Give the extent of all uninfected red blood cells.
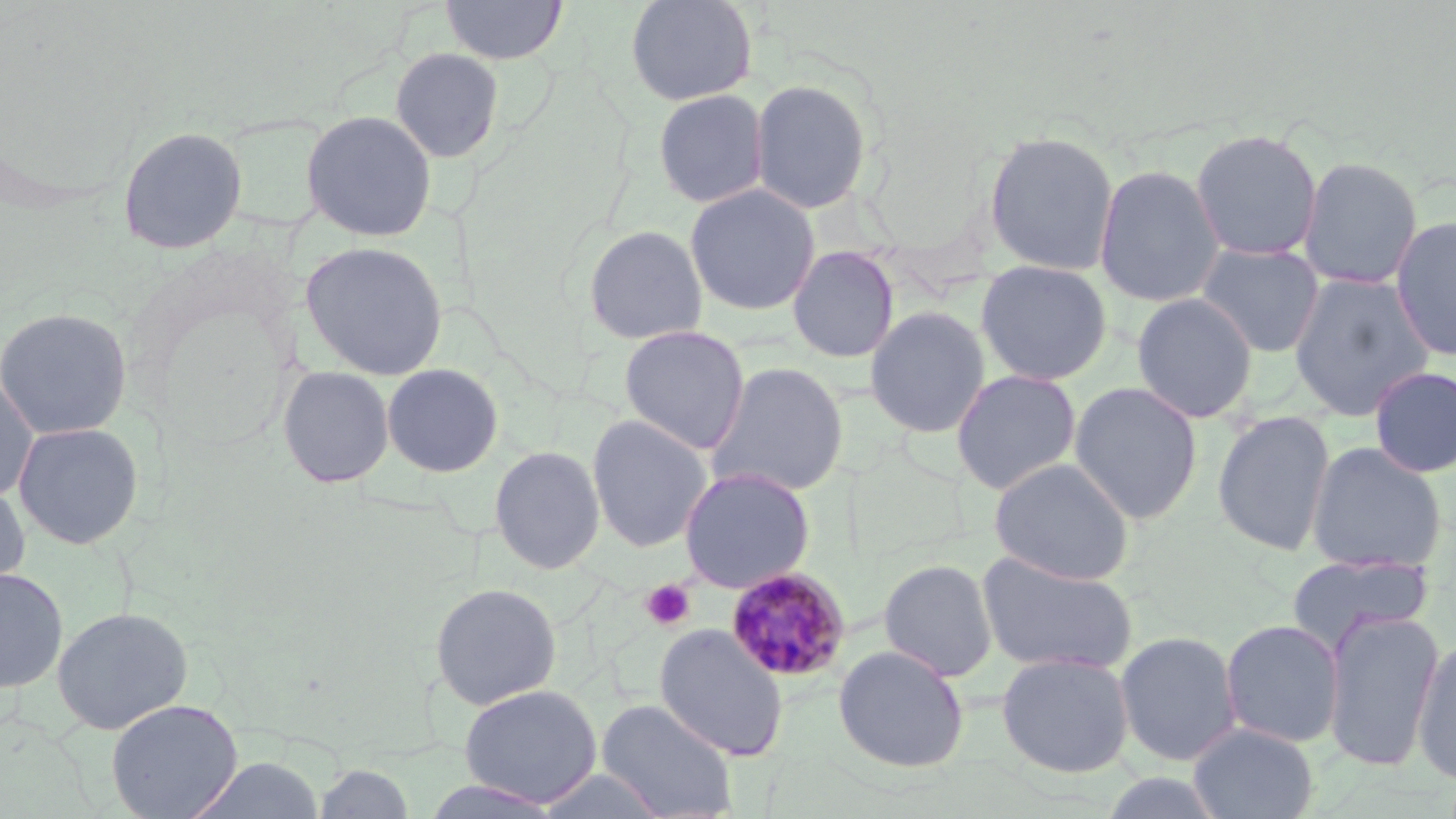
Approximate bounding boxes as (x1,y1)-(x2,y2) corner pairs in pixels.
Uninfected red blood cells: (439,0)-(568,65), (625,0)-(758,107), (389,47)-(506,164), (749,77)-(873,215), (652,88)-(769,208), (300,109)-(438,242), (118,125)-(248,255), (1189,128)-(1323,261), (982,129)-(1120,276), (1298,156)-(1423,290), (1093,163)-(1225,307), (684,183)-(821,316), (1390,215)-(1456,361), (581,224)-(709,345), (300,241)-(449,380), (1196,242)-(1325,357), (787,246)-(900,363), (974,259)-(1113,385), (1289,272)-(1434,421), (1132,292)-(1258,424), (864,305)-(990,438), (0,307)-(133,440), (618,325)-(750,455), (705,360)-(849,498), (381,363)-(503,478), (277,365)-(395,488), (1369,366)-(1456,478), (950,368)-(1082,495), (0,373)-(39,502), (1069,380)-(1204,524), (1212,408)-(1336,557), (587,414)-(712,553), (12,421)-(145,550), (1306,441)-(1447,572), (488,445)-(606,575), (988,457)-(1135,585), (678,466)-(815,593), (0,479)-(31,595), (976,552)-(1138,676), (1287,552)-(1433,650), (879,558)-(998,682), (0,567)-(68,694), (429,582)-(562,710), (52,606)-(193,734), (1322,608)-(1444,773), (1220,619)-(1345,748), (654,624)-(789,761), (1114,630)-(1242,767), (1412,638)-(1456,785), (832,644)-(970,773), (996,651)-(1136,778), (459,683)-(602,807), (105,698)-(244,819), (596,699)-(737,819), (1188,723)-(1319,819), (183,753)-(326,819), (534,768)-(670,819).

{
  "slide_level_diagnosis": "Plasmodium malariae",
  "field_of_view": "single",
  "magnification": "1000x",
  "modality": "optical microscopy",
  "plasmodium_malariae_infected_red_blood_cell_locations": "approximate bounding boxes as (x1,y1)-(x2,y2) corner pairs in pixels: (724,567)-(851,684)",
  "platelet_locations": "approximate bounding boxes as (x1,y1)-(x2,y2) corner pairs in pixels: (640,579)-(695,630)",
  "image_size": "1456×819 pixels",
  "stain": "May-Grünwald-Giemsa",
  "preparation": "thin blood film"
}